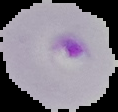 Result: Plasmodium parasites identified. Image is 118×112 pixels. From a thin blood smear. The area outside the segmented cell region is set to black.